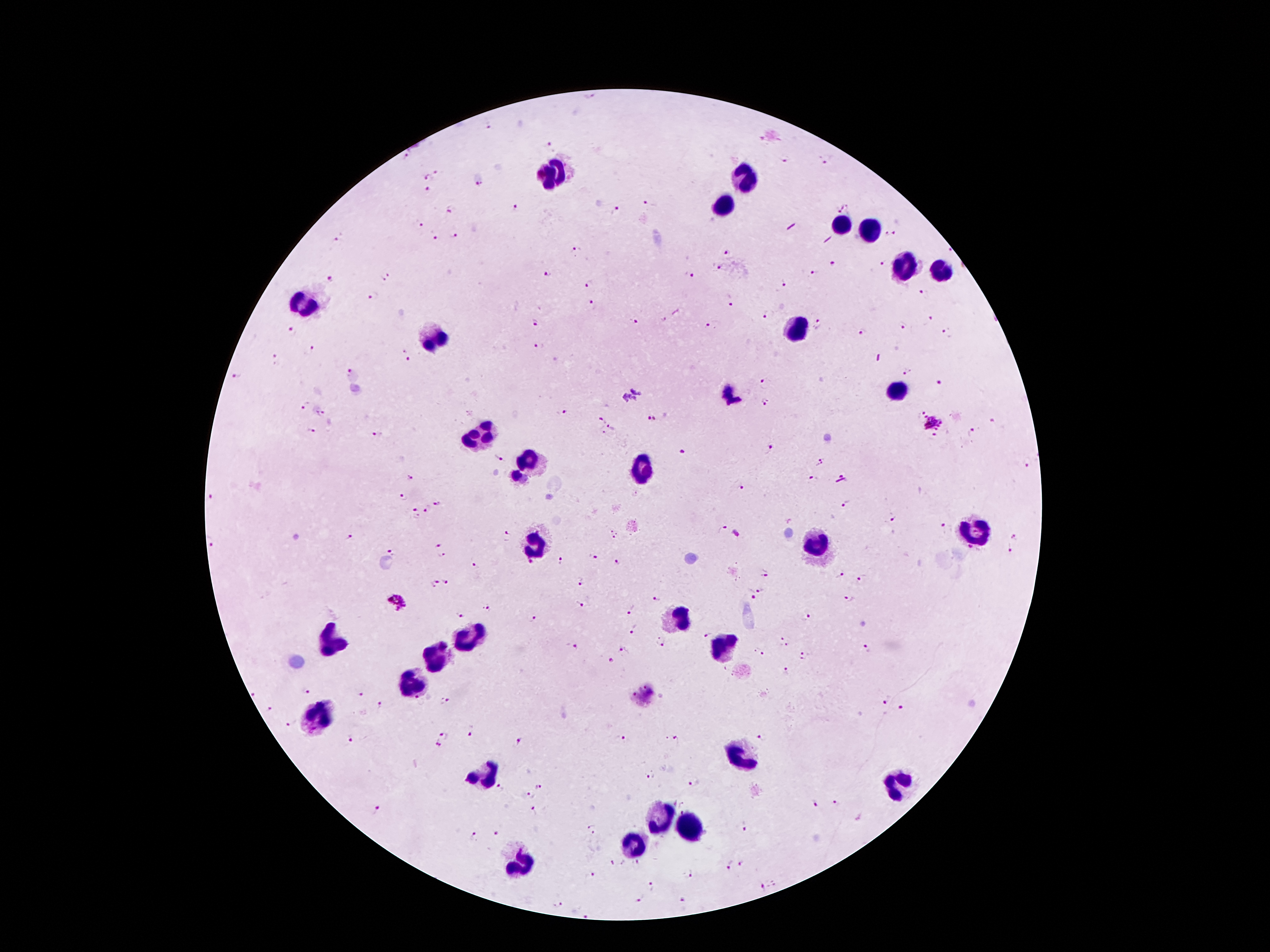

coordinate format = approximate centers as (x, y) in pixels
Plasmodium parasite locations = (591, 97), (488, 126), (551, 145), (407, 155), (825, 160), (784, 161), (439, 173), (427, 176), (479, 185), (427, 190), (649, 204), (515, 209), (842, 209), (450, 210), (616, 211), (419, 224), (891, 234), (455, 235), (436, 238), (339, 240), (577, 250), (728, 252), (834, 263), (883, 263), (718, 268), (549, 272), (813, 272), (688, 273), (386, 276), (333, 277), (785, 282), (588, 284), (923, 293), (374, 296), (731, 299), (591, 304), (767, 314), (930, 318), (634, 320), (535, 322), (712, 324), (819, 324), (904, 326), (292, 332), (861, 332), (947, 335), (541, 345), (311, 349), (406, 355), (276, 358), (905, 370), (348, 372), (239, 377), (766, 383), (939, 383), (767, 402), (306, 405), (564, 411), (919, 412), (322, 414), (652, 420), (603, 421), (932, 422), (993, 422), (612, 428), (311, 430), (973, 433), (377, 434), (932, 439), (769, 447), (684, 453), (498, 459), (1028, 462), (819, 463), (410, 478), (813, 478), (740, 488), (403, 497), (211, 499), (439, 503), (845, 505), (427, 509), (415, 513), (893, 520), (945, 526), (722, 529), (614, 534), (505, 536), (348, 537), (1014, 537), (211, 545), (438, 546), (1009, 547), (970, 548), (390, 551), (441, 556), (592, 557), (561, 560), (617, 563), (530, 564), (476, 567), (764, 573), (839, 576), (861, 579), (436, 583), (447, 583), (580, 583), (759, 591), (751, 594), (850, 597), (658, 599), (398, 601), (581, 603), (487, 607), (630, 611), (456, 615), (807, 618), (533, 619), (633, 630), (706, 636), (784, 641), (661, 642), (572, 647), (867, 649), (624, 650), (759, 652), (803, 656), (612, 660), (785, 670), (644, 687), (306, 690), (255, 695), (361, 695), (634, 695), (418, 700), (444, 700), (885, 700), (380, 706), (269, 709), (903, 709), (291, 723), (446, 736), (471, 736), (761, 737), (624, 739), (677, 739), (350, 742), (519, 742), (437, 746), (651, 775), (539, 785), (693, 785), (501, 788), (530, 796), (815, 804), (837, 804), (378, 811), (535, 812), (745, 827), (591, 831), (497, 834), (473, 836), (613, 862), (742, 864), (729, 865), (594, 875), (690, 875), (653, 886), (762, 887), (641, 900), (684, 901), (558, 904), (586, 915)
leukocyte locations = (553, 172), (747, 174), (721, 206), (837, 227), (865, 232), (907, 262), (941, 272), (305, 305), (795, 329), (433, 337), (897, 386), (477, 436), (527, 464), (641, 472), (975, 530), (535, 544), (815, 546), (675, 621), (467, 636), (331, 641), (725, 649), (437, 659), (411, 683), (319, 713), (741, 750), (481, 773), (895, 790), (655, 820), (685, 829), (629, 847), (523, 863)
patient malaria status = positive for Plasmodium falciparum
magnification = 100x
capture = smartphone through the microscope eyepiece
field of view = single
image size = 1270×952 pixels
preparation = thick peripheral-blood smear
stain = Giemsa